Classify this cell by malaria status.
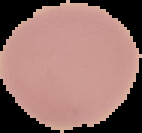
It is uninfected.

Summary:
  - Preparation: thin blood smear
  - Image size: 142×133 pixels
  - Image type: segmented cell region with the area outside set to black